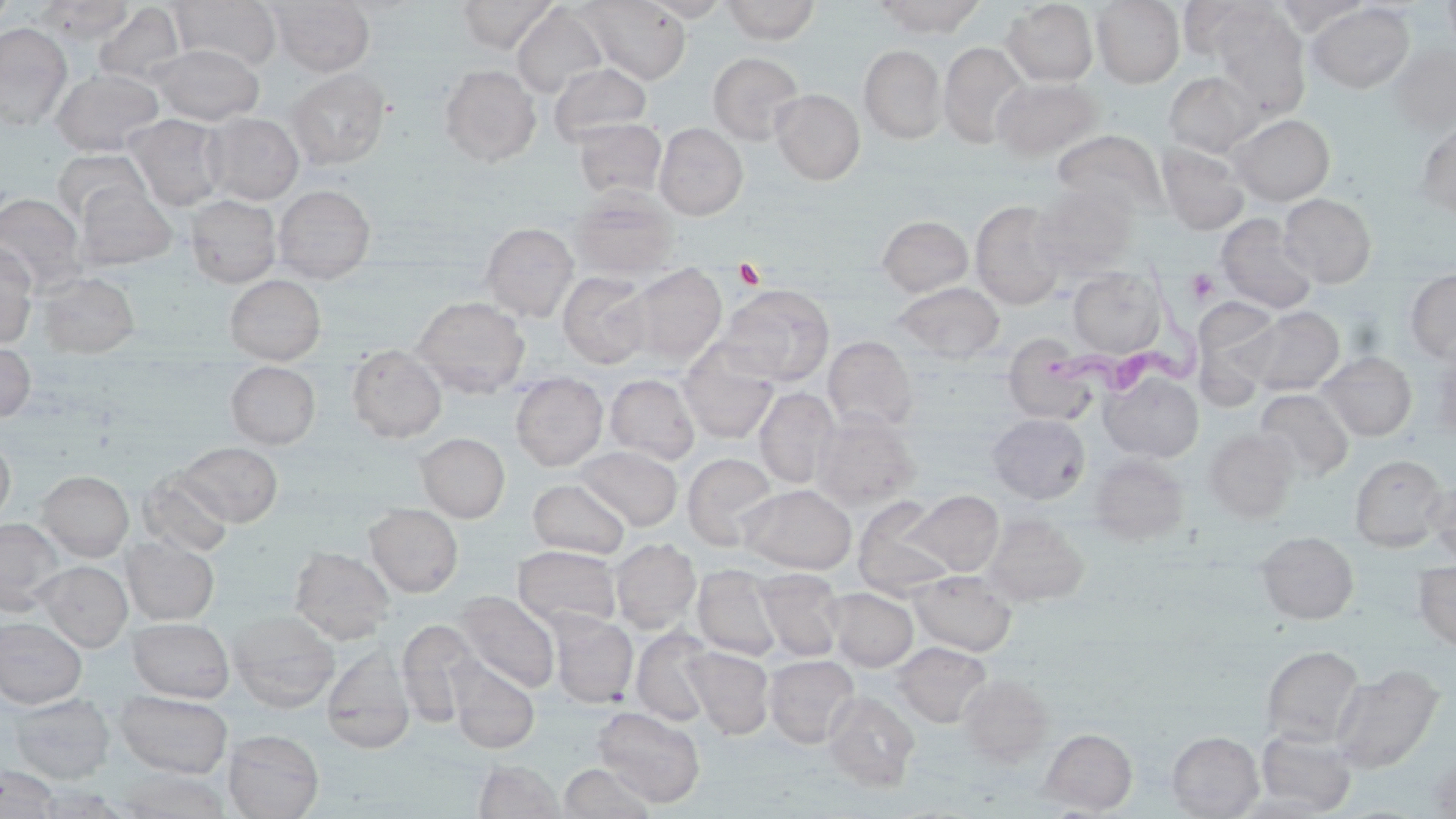
Approximate bounding boxes as named x1/y1/x2/y2 corners in pixels. Trypanosoma brucei locations: (x1=1038, y1=257, x2=1215, y2=401). Uninfected red blood cell locations: (x1=0, y1=0, x2=16, y2=25), (x1=39, y1=0, x2=132, y2=43), (x1=267, y1=0, x2=374, y2=76), (x1=457, y1=0, x2=559, y2=53), (x1=580, y1=0, x2=691, y2=84), (x1=640, y1=0, x2=731, y2=21), (x1=720, y1=0, x2=821, y2=43), (x1=874, y1=0, x2=987, y2=37), (x1=1092, y1=0, x2=1185, y2=87), (x1=1177, y1=0, x2=1272, y2=61), (x1=1442, y1=0, x2=1456, y2=58), (x1=169, y1=1, x2=281, y2=71), (x1=1002, y1=1, x2=1098, y2=86), (x1=1272, y1=1, x2=1371, y2=35), (x1=94, y1=3, x2=186, y2=86), (x1=1306, y1=3, x2=1415, y2=93), (x1=511, y1=4, x2=608, y2=99), (x1=1210, y1=6, x2=1311, y2=116), (x1=0, y1=23, x2=72, y2=131), (x1=938, y1=42, x2=1031, y2=149), (x1=1387, y1=43, x2=1456, y2=135), (x1=151, y1=44, x2=263, y2=125), (x1=859, y1=45, x2=946, y2=144), (x1=707, y1=52, x2=805, y2=144), (x1=549, y1=61, x2=652, y2=147), (x1=440, y1=65, x2=541, y2=166), (x1=51, y1=68, x2=164, y2=156), (x1=285, y1=68, x2=391, y2=169), (x1=1163, y1=71, x2=1261, y2=158), (x1=991, y1=77, x2=1104, y2=161), (x1=771, y1=89, x2=865, y2=184), (x1=203, y1=113, x2=304, y2=204), (x1=1228, y1=113, x2=1335, y2=206), (x1=127, y1=114, x2=226, y2=211), (x1=573, y1=118, x2=666, y2=200), (x1=1415, y1=118, x2=1456, y2=221), (x1=654, y1=122, x2=748, y2=220), (x1=1052, y1=129, x2=1168, y2=220), (x1=1156, y1=142, x2=1250, y2=235), (x1=52, y1=149, x2=151, y2=226), (x1=1031, y1=183, x2=1138, y2=278), (x1=274, y1=184, x2=375, y2=282), (x1=75, y1=185, x2=178, y2=270), (x1=570, y1=190, x2=680, y2=280), (x1=0, y1=193, x2=86, y2=292), (x1=1279, y1=193, x2=1377, y2=288), (x1=185, y1=194, x2=281, y2=287), (x1=970, y1=200, x2=1067, y2=310), (x1=1215, y1=214, x2=1318, y2=314), (x1=877, y1=215, x2=973, y2=297), (x1=481, y1=222, x2=579, y2=321), (x1=0, y1=243, x2=37, y2=348), (x1=625, y1=264, x2=727, y2=366), (x1=1068, y1=266, x2=1166, y2=357), (x1=1404, y1=268, x2=1456, y2=363), (x1=36, y1=270, x2=140, y2=357), (x1=558, y1=271, x2=653, y2=368), (x1=225, y1=274, x2=326, y2=365), (x1=893, y1=282, x2=1005, y2=364), (x1=719, y1=284, x2=834, y2=385), (x1=412, y1=296, x2=530, y2=397), (x1=1195, y1=303, x2=1281, y2=403), (x1=1243, y1=306, x2=1345, y2=397), (x1=823, y1=335, x2=918, y2=431), (x1=1002, y1=338, x2=1099, y2=426), (x1=0, y1=340, x2=35, y2=422), (x1=346, y1=344, x2=446, y2=442), (x1=678, y1=344, x2=780, y2=443), (x1=1427, y1=344, x2=1456, y2=443), (x1=1318, y1=351, x2=1417, y2=440), (x1=226, y1=361, x2=321, y2=449), (x1=510, y1=372, x2=608, y2=470), (x1=1101, y1=372, x2=1203, y2=462), (x1=605, y1=373, x2=700, y2=465), (x1=755, y1=387, x2=839, y2=489), (x1=1255, y1=388, x2=1353, y2=483), (x1=812, y1=412, x2=921, y2=510), (x1=988, y1=413, x2=1090, y2=503), (x1=1204, y1=428, x2=1298, y2=522), (x1=0, y1=432, x2=16, y2=525), (x1=416, y1=432, x2=510, y2=522), (x1=175, y1=442, x2=283, y2=526), (x1=575, y1=445, x2=682, y2=531), (x1=683, y1=452, x2=780, y2=550), (x1=1089, y1=454, x2=1189, y2=544), (x1=1350, y1=454, x2=1450, y2=550), (x1=38, y1=470, x2=134, y2=560), (x1=140, y1=470, x2=234, y2=557), (x1=1425, y1=473, x2=1456, y2=565), (x1=528, y1=478, x2=630, y2=558), (x1=738, y1=483, x2=857, y2=574), (x1=901, y1=489, x2=1004, y2=576), (x1=852, y1=497, x2=955, y2=596), (x1=365, y1=503, x2=463, y2=597), (x1=982, y1=514, x2=1089, y2=606), (x1=0, y1=518, x2=65, y2=615), (x1=1256, y1=531, x2=1359, y2=624), (x1=121, y1=536, x2=220, y2=625), (x1=609, y1=538, x2=700, y2=633), (x1=512, y1=545, x2=622, y2=632), (x1=290, y1=546, x2=394, y2=644), (x1=34, y1=560, x2=132, y2=651), (x1=1413, y1=560, x2=1456, y2=651), (x1=693, y1=564, x2=783, y2=660), (x1=754, y1=569, x2=845, y2=662), (x1=910, y1=570, x2=1017, y2=655), (x1=825, y1=587, x2=918, y2=671), (x1=456, y1=590, x2=560, y2=692), (x1=228, y1=610, x2=341, y2=712), (x1=550, y1=613, x2=638, y2=707), (x1=0, y1=617, x2=87, y2=708), (x1=128, y1=617, x2=234, y2=702), (x1=397, y1=619, x2=479, y2=719), (x1=631, y1=627, x2=717, y2=725), (x1=893, y1=642, x2=991, y2=727), (x1=1261, y1=645, x2=1365, y2=747), (x1=683, y1=646, x2=774, y2=739), (x1=321, y1=648, x2=416, y2=752), (x1=764, y1=654, x2=859, y2=747), (x1=447, y1=658, x2=540, y2=753), (x1=1331, y1=664, x2=1445, y2=774), (x1=957, y1=674, x2=1053, y2=767), (x1=114, y1=690, x2=233, y2=778), (x1=823, y1=691, x2=919, y2=791), (x1=8, y1=694, x2=115, y2=783), (x1=593, y1=706, x2=706, y2=807), (x1=1041, y1=728, x2=1137, y2=814), (x1=223, y1=729, x2=324, y2=819), (x1=1255, y1=729, x2=1356, y2=815), (x1=1167, y1=731, x2=1263, y2=818), (x1=1427, y1=754, x2=1456, y2=817), (x1=475, y1=760, x2=564, y2=819), (x1=559, y1=763, x2=656, y2=819), (x1=0, y1=765, x2=60, y2=818), (x1=114, y1=769, x2=230, y2=818). Platelet locations: (x1=735, y1=260, x2=767, y2=290), (x1=1185, y1=268, x2=1219, y2=305). Slide-level diagnosis: Trypanosoma brucei. Light microscopy. Image is 1456×819 pixels. Single field of view. May-Grünwald-Giemsa stain. Thin blood smear. 1000x magnification.